Outline platelets.
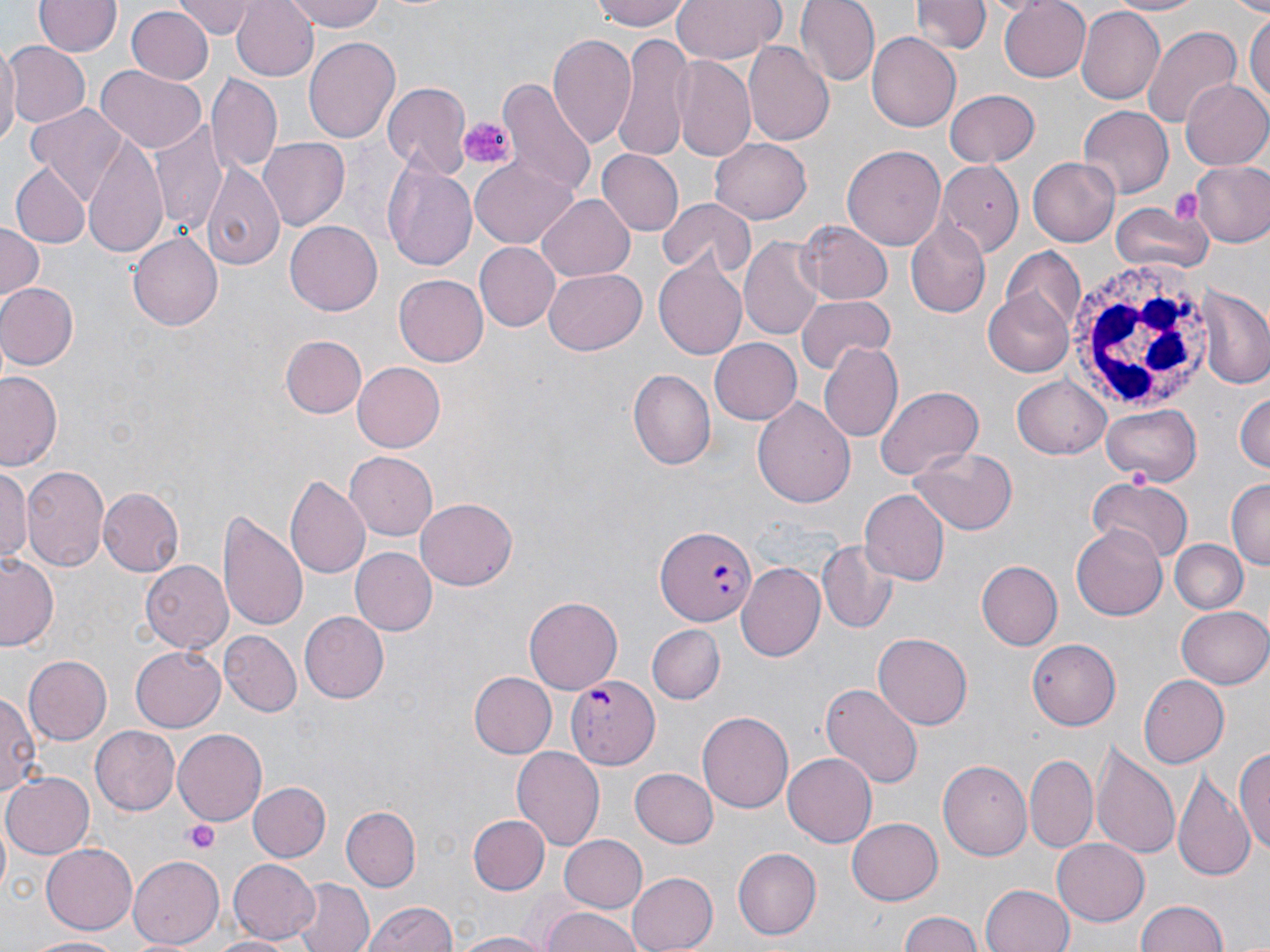
Approximate bounding boxes as (x1,y1)-(x2,y2) corner pairs in pixels.
Platelets: (458,116)-(515,168), (1169,186)-(1206,227), (184,822)-(219,855).

Summary:
  - White blood cell locations: (1063,256)-(1218,420)
  - Uninfected red blood cell locations: (36,0)-(119,57), (179,0)-(259,37), (231,0)-(322,81), (283,0)-(388,31), (593,0)-(695,31), (669,0)-(785,65), (794,0)-(877,87), (913,0)-(987,54), (996,0)-(1092,81), (1104,0)-(1207,16), (1076,6)-(1164,107), (124,7)-(213,86), (1245,8)-(1269,115), (1141,24)-(1243,130), (866,31)-(960,131), (613,33)-(691,160), (548,34)-(638,151), (303,35)-(400,145), (743,40)-(834,148), (1,42)-(88,130), (0,45)-(19,149), (673,56)-(755,160), (95,68)-(205,154), (207,75)-(283,175), (499,75)-(598,204), (1181,78)-(1270,171), (382,81)-(470,179), (945,88)-(1040,167), (25,102)-(133,204), (1078,106)-(1173,197), (148,123)-(226,237), (258,137)-(348,231), (82,138)-(170,257), (709,138)-(813,224), (845,145)-(945,254), (597,149)-(683,235), (1027,156)-(1120,247), (470,159)-(575,246), (1189,159)-(1270,248), (936,160)-(1021,253), (10,162)-(87,246), (201,162)-(286,275), (385,162)-(477,275), (538,197)-(634,279), (657,197)-(755,278), (1111,200)-(1215,273), (903,216)-(991,320), (285,221)-(382,314), (0,223)-(43,305), (799,223)-(894,308), (130,230)-(225,330), (740,233)-(826,343), (472,242)-(559,331), (999,247)-(1086,338), (655,258)-(751,359), (544,266)-(646,354), (393,273)-(488,366), (0,282)-(78,370), (1198,286)-(1270,389), (982,290)-(1076,377), (794,296)-(895,375), (279,335)-(367,419), (709,336)-(802,423), (819,340)-(904,443), (354,361)-(447,452), (1,369)-(64,472), (628,369)-(717,471), (1013,375)-(1110,458), (876,385)-(984,481), (1233,389)-(1270,478), (754,396)-(854,511), (1102,403)-(1202,486), (908,448)-(1018,534), (344,451)-(439,539), (21,463)-(110,574), (0,468)-(32,567), (286,474)-(368,579), (1086,478)-(1192,564), (1228,478)-(1270,568), (97,487)-(183,576), (859,489)-(949,584), (416,498)-(517,590), (218,510)-(307,632), (1071,526)-(1168,621), (1172,540)-(1249,614), (817,542)-(899,632), (350,548)-(434,636), (0,553)-(59,651), (138,561)-(234,653), (977,561)-(1063,650), (737,562)-(826,663), (525,596)-(622,695), (1177,605)-(1269,688), (299,612)-(387,703), (647,625)-(725,703), (218,630)-(303,717), (872,633)-(973,730), (1026,638)-(1121,731), (132,646)-(225,731), (24,655)-(111,743), (469,672)-(556,758), (1137,675)-(1228,769), (819,682)-(924,790), (0,685)-(41,797), (697,711)-(794,814), (88,725)-(180,815), (173,731)-(267,823), (1091,742)-(1181,863), (1234,744)-(1270,860), (512,745)-(605,848), (784,753)-(878,847), (1026,754)-(1099,853), (938,759)-(1032,862), (1173,768)-(1256,883), (629,769)-(718,849), (1,770)-(93,859), (248,781)-(331,862), (343,806)-(420,892), (468,814)-(550,894), (847,817)-(944,905), (560,834)-(647,911), (1053,838)-(1150,924), (42,842)-(138,933), (733,847)-(822,940), (128,855)-(225,948), (229,858)-(320,944), (626,871)-(718,952), (291,878)-(371,952), (980,882)-(1075,952), (1135,898)-(1230,952), (359,900)-(459,952), (540,908)-(646,952), (897,912)-(989,952), (452,931)-(554,951), (28,934)-(125,952), (204,934)-(295,952)
  - Plasmodium falciparum-infected red blood cell locations: (654,522)-(759,626), (567,675)-(661,770)
  - Slide-level diagnosis: Plasmodium falciparum
  - Preparation: thin blood film
  - Magnification: 1000x
  - Stain: May-Grünwald-Giemsa
  - Field of view: single
  - Modality: light microscopy
  - Image size: 1270×952 pixels